Comment on the morphology of the red blood cells.
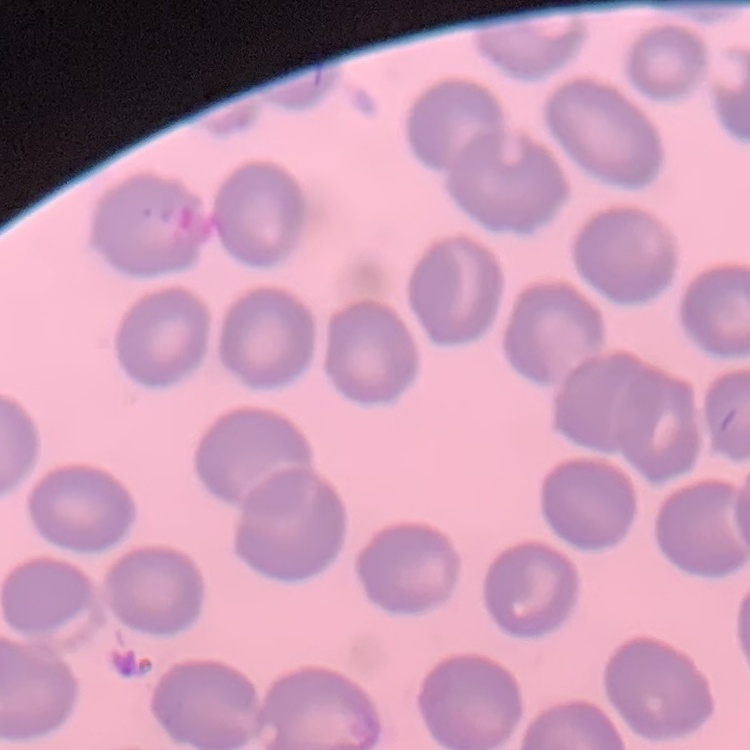

They show no rouleaux formation.

preparation = thin peripheral smear
stain = Field's or Giemsa
image type = square crop of a larger photomicrograph